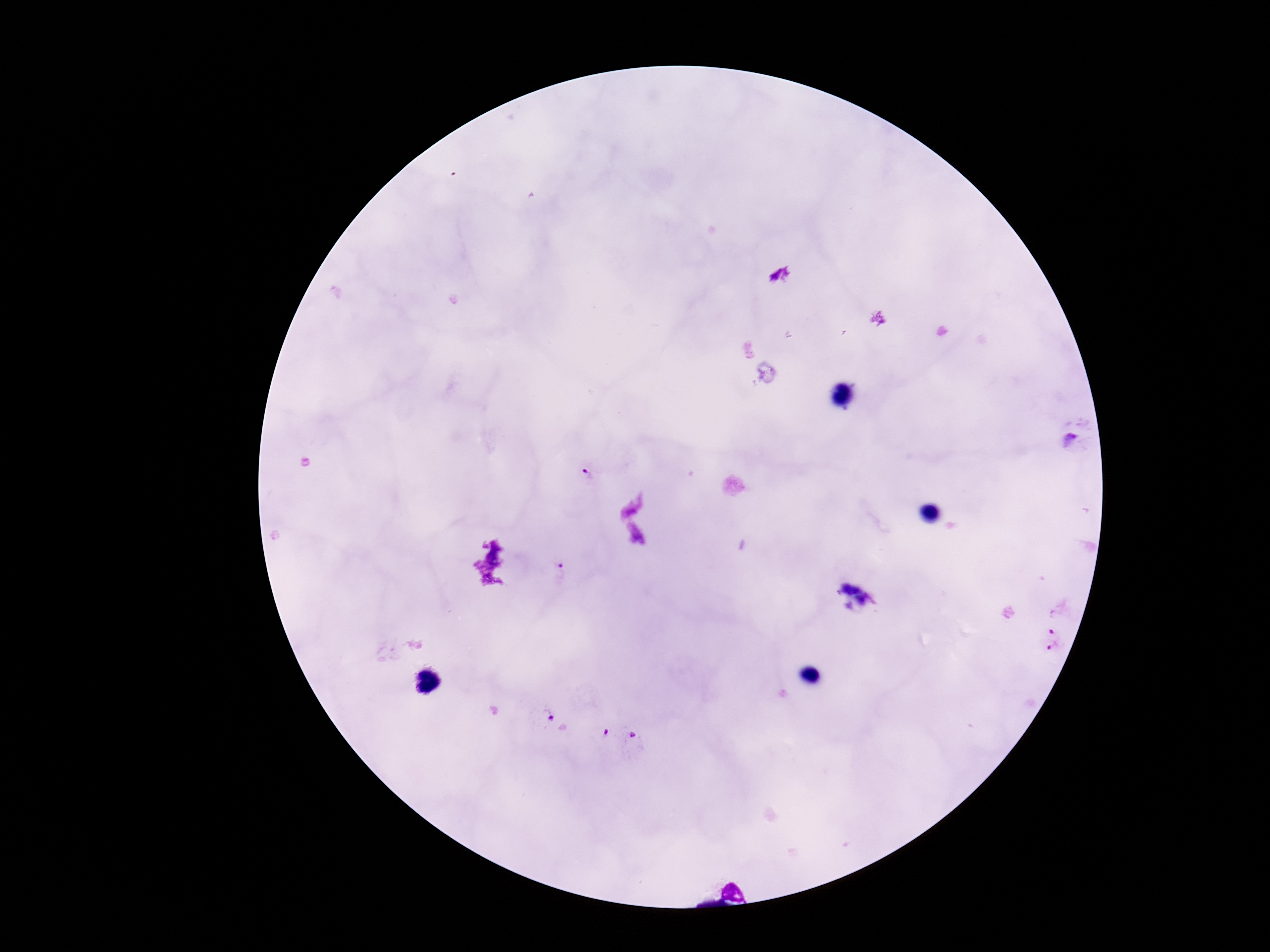

Approximate centers as [x, y] in pixels.
Summary:
  - Plasmodium parasite locations: [1070, 439], [588, 478], [562, 566], [1055, 625], [1053, 649], [543, 715], [604, 739], [641, 742]
  - Image size: 1270×952 pixels
  - Stain: Giemsa
  - Field of view: single
  - Capture: smartphone camera through the microscope eyepiece
  - Patient malaria status: infected
  - Preparation: thick peripheral-blood smear
  - Magnification: 100x